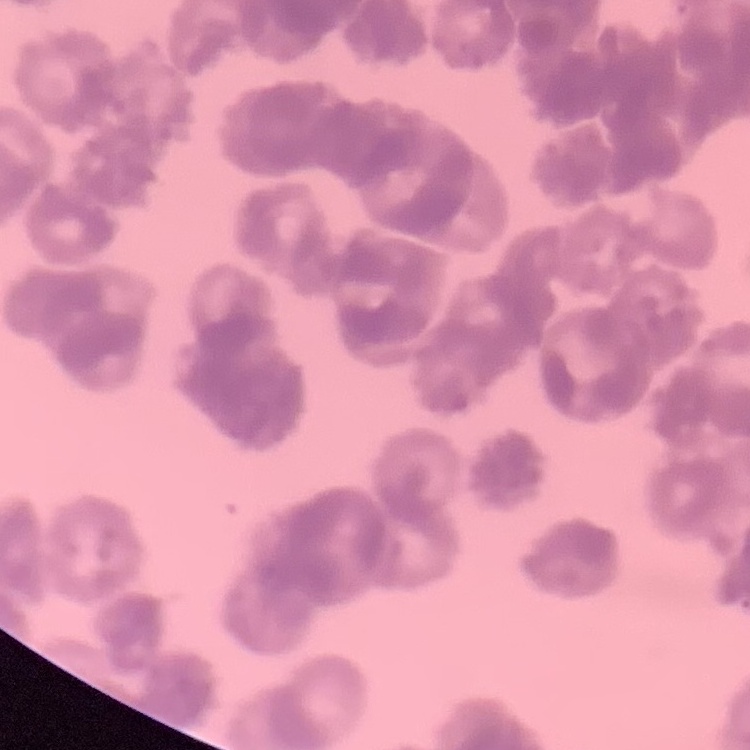 The red blood cells exhibit rouleaux formation. Thin blood film. One tile cut from a larger photomicrograph. Field's or Giemsa stain.